Describe the morphology of the erythrocytes.
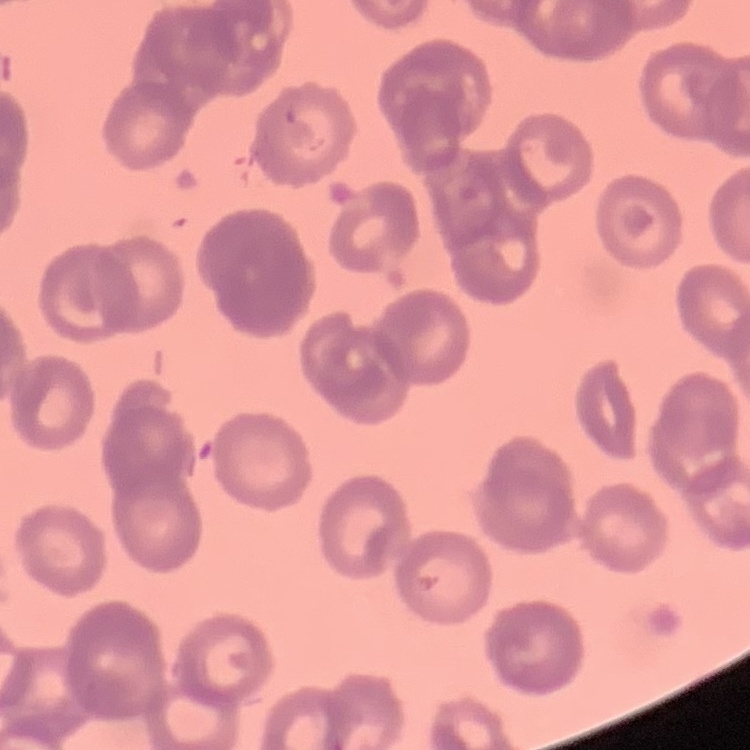

Rouleaux formation.

{
  "image_type": "square crop of a larger photomicrograph",
  "stain": "Field's or Giemsa",
  "preparation": "thin peripheral smear"
}